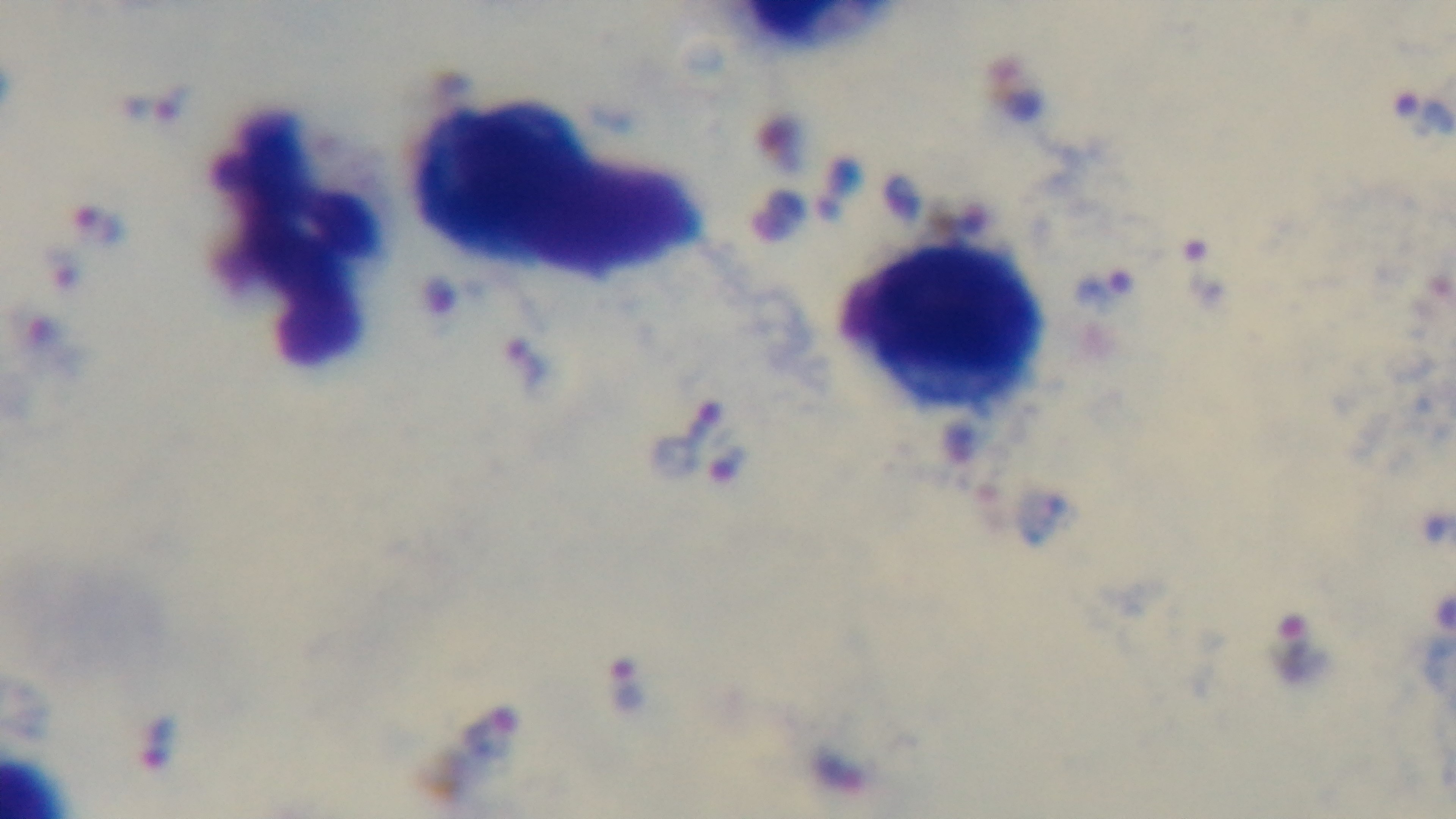
objective = 100x oil immersion
modality = light microscopy
field of view = one from the slide
preparation = thick
stain = Giemsa
malaria status = infected
capture = mounted 4K digital camera